Assess this cell for malaria.
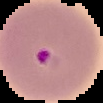
Parasitized.

image_size: 103×103 pixels
image_type: cell region segmented out of the field of view; surrounding area masked to black
preparation: thin blood film